State the blood parasite species.
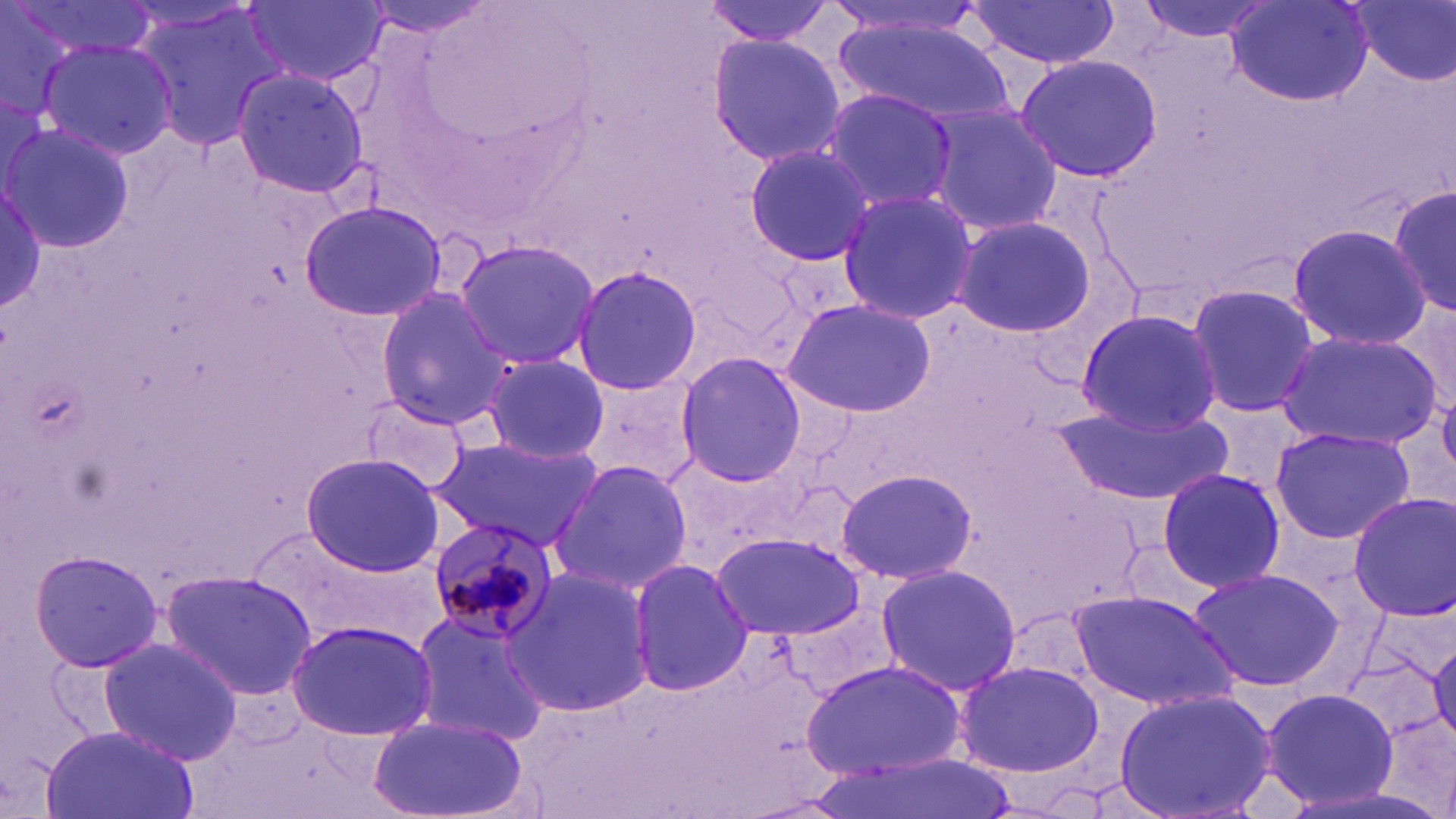
Plasmodium malariae.

uninfected_red_blood_cell_locations: 'approximate bounding boxes as named x1/y1/x2/y2 corners in pixels: (x1=1, y1=0, x2=88, y2=123), (x1=12, y1=0, x2=157, y2=61), (x1=244, y1=0, x2=389, y2=88), (x1=357, y1=0, x2=498, y2=35), (x1=703, y1=0, x2=842, y2=45), (x1=1131, y1=0, x2=1282, y2=42), (x1=1226, y1=0, x2=1371, y2=107), (x1=820, y1=1, x2=989, y2=39), (x1=964, y1=1, x2=1124, y2=70), (x1=1348, y1=1, x2=1454, y2=88), (x1=132, y1=2, x2=293, y2=155), (x1=828, y1=15, x2=1020, y2=123), (x1=706, y1=32, x2=845, y2=168), (x1=37, y1=36, x2=178, y2=161), (x1=1013, y1=53, x2=1161, y2=180), (x1=231, y1=66, x2=372, y2=199), (x1=821, y1=90, x2=956, y2=209), (x1=917, y1=102, x2=1063, y2=239), (x1=4, y1=122, x2=134, y2=251), (x1=741, y1=141, x2=878, y2=267), (x1=0, y1=179, x2=48, y2=317), (x1=1384, y1=180, x2=1455, y2=321), (x1=835, y1=189, x2=979, y2=323), (x1=301, y1=201, x2=446, y2=321), (x1=951, y1=215, x2=1097, y2=338), (x1=1285, y1=223, x2=1433, y2=350), (x1=452, y1=236, x2=599, y2=370), (x1=574, y1=264, x2=702, y2=395), (x1=1185, y1=282, x2=1321, y2=420), (x1=375, y1=287, x2=513, y2=428), (x1=781, y1=298, x2=936, y2=418), (x1=1075, y1=310, x2=1220, y2=434), (x1=1276, y1=329, x2=1444, y2=451), (x1=477, y1=351, x2=610, y2=464), (x1=672, y1=352, x2=807, y2=488), (x1=575, y1=372, x2=700, y2=495), (x1=1438, y1=385, x2=1456, y2=481), (x1=359, y1=396, x2=472, y2=493), (x1=1057, y1=403, x2=1229, y2=509), (x1=1269, y1=424, x2=1414, y2=546), (x1=429, y1=435, x2=601, y2=553), (x1=300, y1=452, x2=445, y2=576), (x1=550, y1=458, x2=695, y2=597), (x1=832, y1=466, x2=979, y2=586), (x1=1155, y1=466, x2=1285, y2=595), (x1=1346, y1=493, x2=1456, y2=619), (x1=239, y1=523, x2=430, y2=650), (x1=712, y1=533, x2=865, y2=640), (x1=26, y1=547, x2=164, y2=673), (x1=628, y1=558, x2=750, y2=698), (x1=876, y1=562, x2=1023, y2=696), (x1=502, y1=565, x2=656, y2=720), (x1=1186, y1=567, x2=1347, y2=694), (x1=160, y1=569, x2=316, y2=697), (x1=1069, y1=589, x2=1242, y2=714), (x1=406, y1=611, x2=552, y2=747), (x1=286, y1=620, x2=440, y2=743), (x1=99, y1=635, x2=242, y2=767), (x1=802, y1=659, x2=965, y2=778), (x1=955, y1=659, x2=1103, y2=777), (x1=1258, y1=684, x2=1402, y2=813), (x1=1112, y1=687, x2=1277, y2=819), (x1=368, y1=712, x2=530, y2=819), (x1=42, y1=723, x2=199, y2=819), (x1=814, y1=755, x2=1009, y2=819)'
plasmodium_malariae_infected_red_blood_cell_locations: 'approximate bounding boxes as named x1/y1/x2/y2 corners in pixels: (x1=424, y1=517, x2=560, y2=645)'
field_of_view: one of a larger specimen
stain: May-Grünwald-Giemsa
image_size: 1456×819 pixels
preparation: thin blood film
modality: light microscopy
magnification: 1000x